Identify the cell.
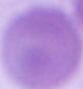
An erythrocyte.

Summary:
  - Modality: micrograph
  - Magnification: 1000x